Locate and identify every blood parasite.
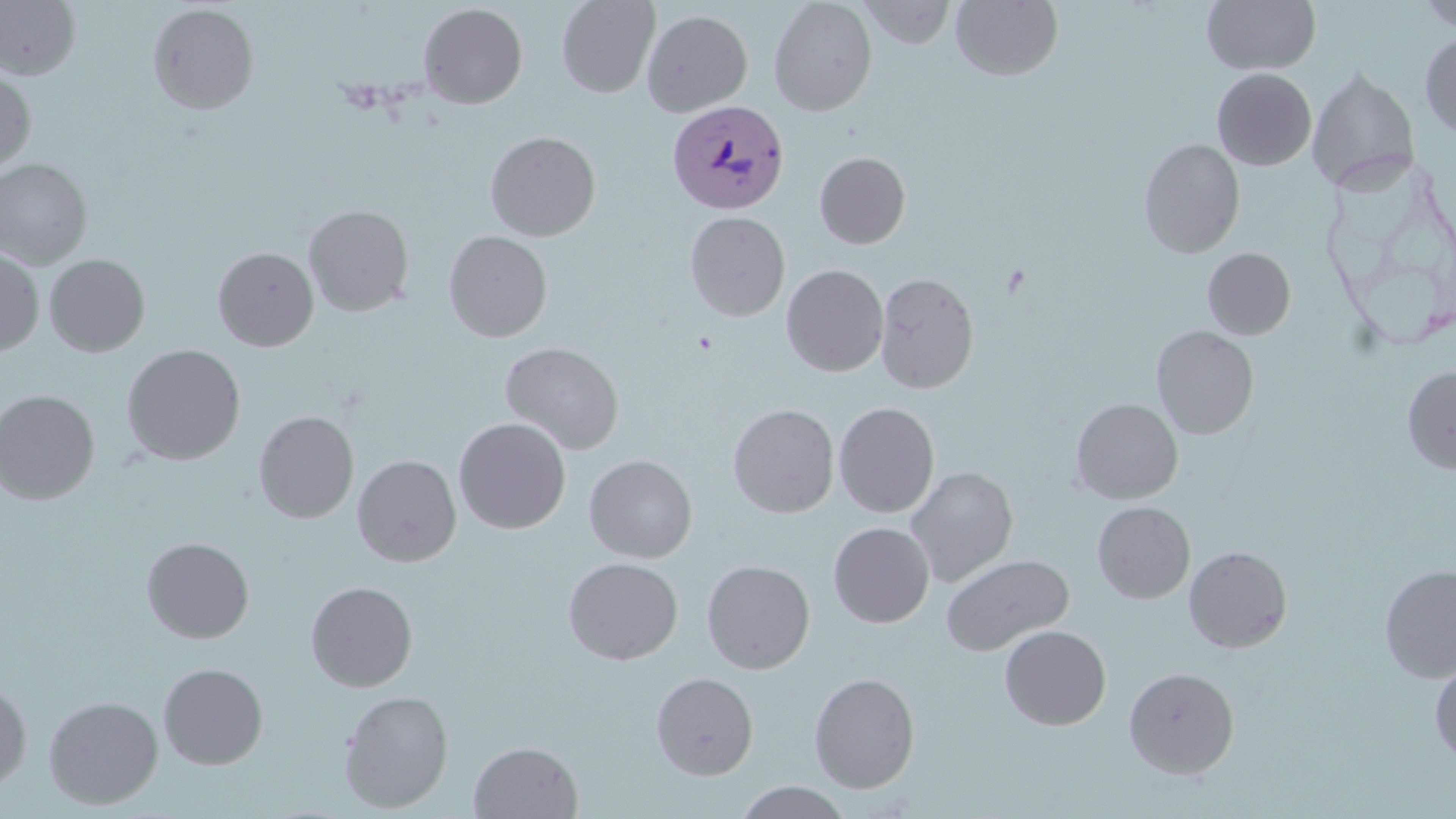
Approximate bounding boxes as [x1, y1, x2, y2] in pixels.
Plasmodium vivax-infected red blood cells: [667, 100, 789, 214].
No Plasmodium falciparum, Plasmodium ovale, Plasmodium malariae, Babesia divergens, or Trypanosoma brucei observed.

Uninfected red blood cell locations: [557, 0, 659, 99], [768, 0, 877, 116], [858, 0, 956, 48], [951, 0, 1063, 81], [1415, 0, 1456, 31], [0, 1, 81, 79], [1202, 1, 1320, 74], [147, 3, 260, 115], [418, 3, 528, 109], [643, 4, 875, 113], [642, 9, 752, 116], [1420, 31, 1456, 138], [1212, 68, 1317, 170], [1307, 68, 1421, 193], [0, 69, 36, 173], [485, 131, 601, 241], [1139, 138, 1245, 258], [815, 152, 911, 248], [0, 158, 93, 268], [303, 204, 415, 317], [685, 212, 790, 321], [443, 231, 553, 342], [212, 246, 319, 351], [0, 247, 44, 356], [1202, 247, 1296, 339], [44, 254, 151, 357], [782, 264, 888, 377], [875, 271, 979, 394], [1152, 325, 1259, 438], [500, 341, 624, 454], [121, 344, 246, 466], [1402, 365, 1456, 474], [0, 388, 101, 505], [1070, 398, 1183, 504], [833, 402, 939, 518], [728, 403, 839, 518], [253, 411, 359, 524], [454, 417, 571, 534], [584, 454, 697, 562], [352, 455, 461, 567], [905, 466, 1018, 587], [1092, 501, 1195, 603], [829, 522, 934, 628], [141, 536, 255, 643], [1184, 545, 1293, 653], [941, 553, 1073, 655], [563, 557, 683, 665], [702, 559, 815, 674], [1379, 563, 1456, 682], [305, 580, 418, 692], [999, 625, 1111, 730], [1429, 659, 1456, 765], [158, 662, 268, 769], [1124, 666, 1240, 778], [650, 671, 758, 780], [809, 672, 920, 793], [0, 679, 32, 794], [338, 689, 454, 812], [43, 695, 163, 810], [468, 740, 584, 818], [734, 781, 855, 818]. Slide-level diagnosis: Plasmodium vivax. May-Grünwald-Giemsa-stained preparation. Single field of view. Thin blood film. Light microscopy. Image is 1456×819 pixels. 1000x magnification.